Assess the morphology of the erythrocytes.
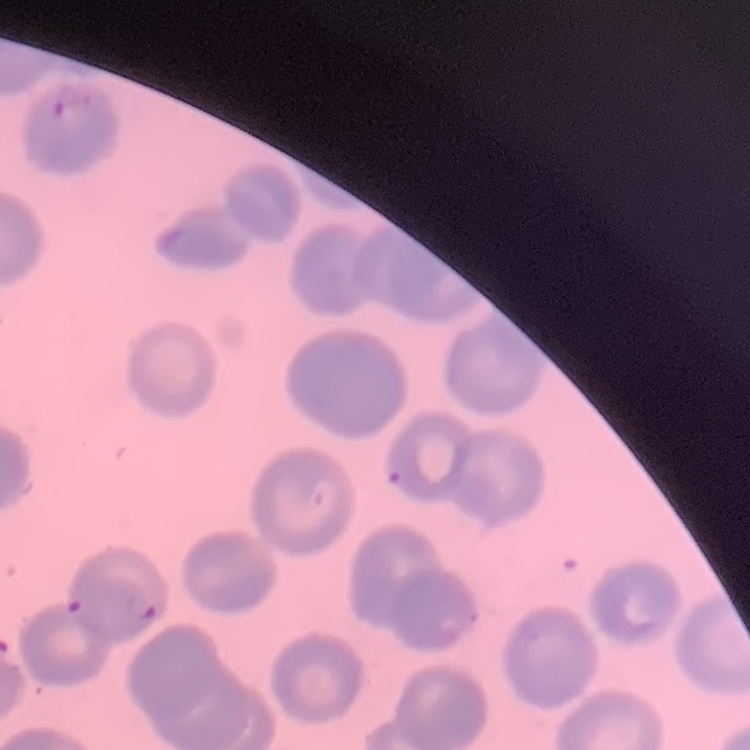
No rouleaux formation.

preparation: thin blood smear
stain: Field's or Giemsa
image_type: square crop of a larger photomicrograph